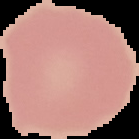

{
  "image_type": "segmented cell region with the area outside set to black",
  "image_size": "139×139 pixels",
  "malaria_status": "uninfected",
  "preparation": "thin blood film"
}